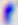

Captured at 400x magnification. Toxoplasma gondii is seen. Micrograph.